Name the cell type shown.
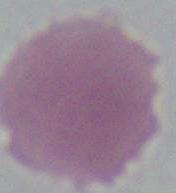

This is an erythrocyte.

Summary:
  - Magnification: 1000x
  - Modality: photomicrograph